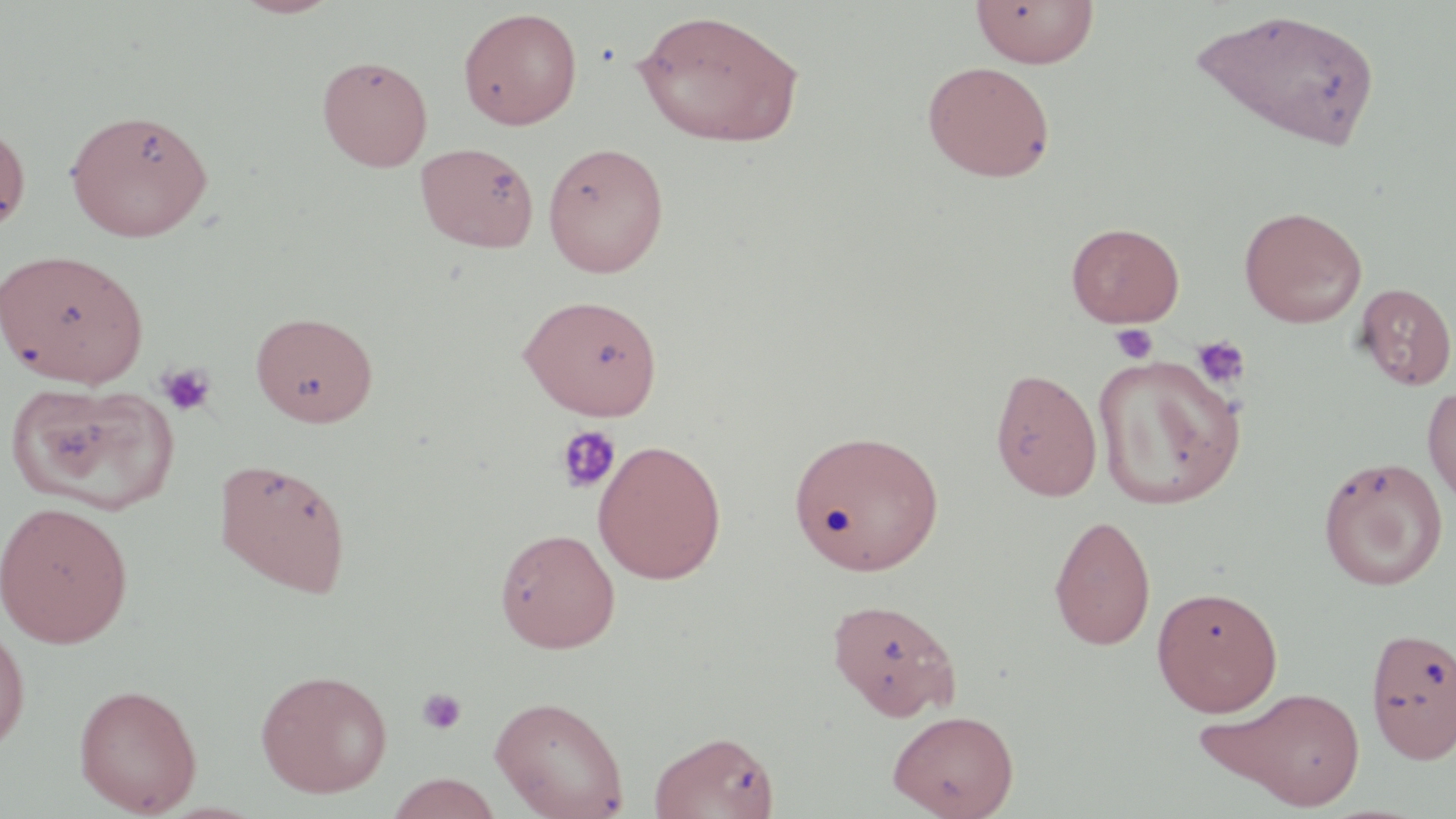
Summary:
  - Coordinate format: approximate bounding boxes as (x1,y1)-(x2,y2) corner pairs in pixels
  - Uninfected red blood cell locations: (233,0)-(342,18), (970,0)-(1099,67), (458,6)-(583,130), (1188,6)-(1384,153), (632,7)-(806,148), (317,55)-(433,172), (921,60)-(1056,183), (65,108)-(214,242), (0,119)-(32,236), (414,141)-(539,253), (542,141)-(669,277), (1238,205)-(1367,327), (1065,222)-(1185,327), (0,247)-(149,388), (1355,282)-(1455,390), (518,293)-(663,419), (250,310)-(378,427), (1092,354)-(1245,509), (989,367)-(1103,501), (7,380)-(177,515), (1422,384)-(1456,512), (787,428)-(944,576), (592,439)-(727,584), (213,455)-(353,598), (1318,456)-(1448,591), (0,500)-(134,648), (1048,514)-(1156,651), (495,527)-(620,653), (1151,585)-(1283,716), (826,597)-(961,721), (0,616)-(30,757), (1364,625)-(1456,764), (255,668)-(392,798), (73,682)-(203,816), (1207,685)-(1368,810), (489,695)-(629,818), (887,709)-(1019,819), (649,729)-(781,818), (384,773)-(502,818)
  - Platelet locations: (1111,323)-(1158,365), (1191,335)-(1251,390), (157,362)-(217,417), (555,424)-(622,495), (417,687)-(468,735)
  - Slide-level diagnosis: no evidence of blood parasites
  - Magnification: 1000x
  - Modality: light microscopy
  - Image size: 1456×819 pixels
  - Stain: May-Grünwald-Giemsa
  - Field of view: one of a larger specimen
  - Preparation: thin blood smear